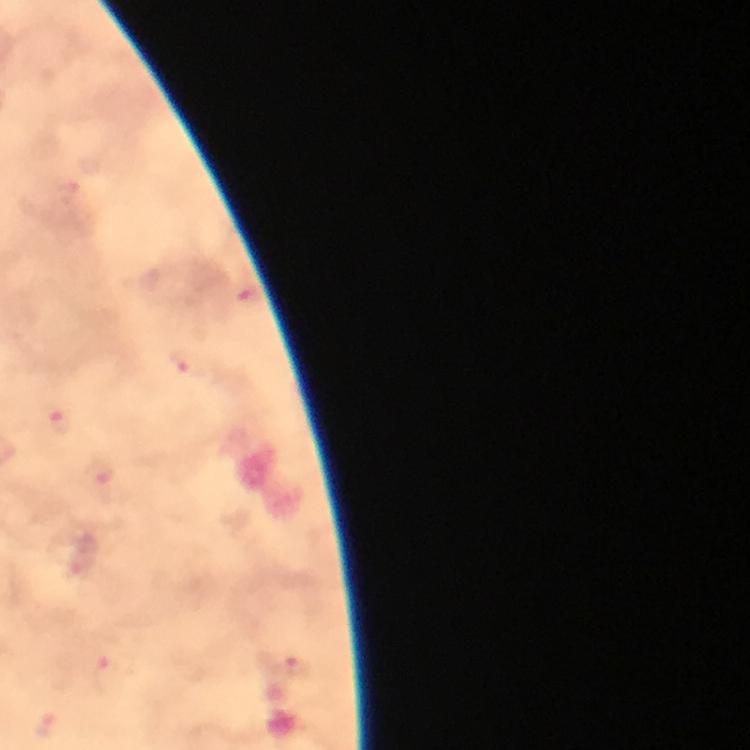

Approximate centers as {x, y} in pixels.
Summary:
  - Plasmodium parasite locations: {184, 363}, {62, 423}, {100, 474}, {298, 666}, {108, 674}, {43, 725}
  - Stain: Giemsa
  - Capture: smartphone camera through the microscope
  - Cropped from: one field of view
  - Context: from a diagnostic examination for malaria
  - Image size: 750×750 pixels
  - Immersion oil: applied
  - Preparation: thick blood smear
  - Magnification: 100x